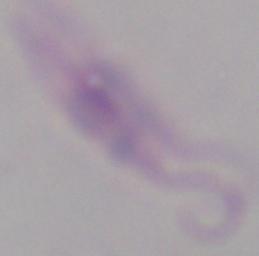

Summary:
  - Identification: Leishmania
  - Modality: photomicrograph
  - Magnification: 1000x